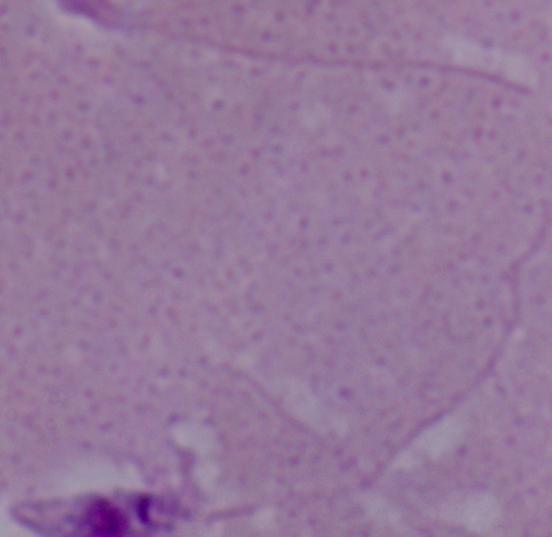
Summary:
  - Magnification: 1000x
  - Identification: Leishmania
  - Modality: photomicrograph